Name the parasite shown.
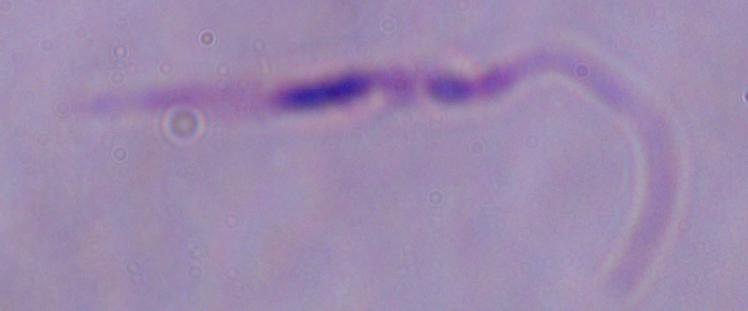
Leishmania.

Captured at 1000x magnification. Micrograph.